Describe the morphology of the erythrocytes.
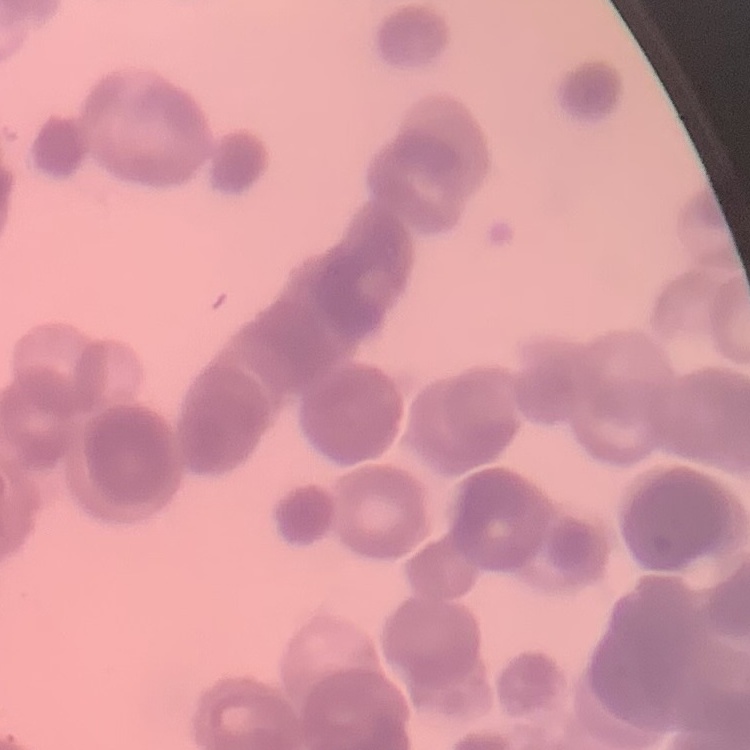

Rouleaux formation.

Field's or Giemsa stain. Thin blood film. Square crop of a larger photomicrograph.